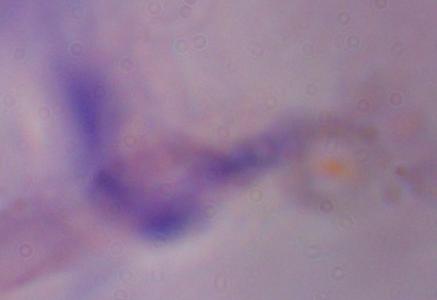
identification = trypanosome
magnification = 1000x
modality = photomicrograph